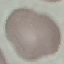
malaria status = uninfected
capture = smartphone through the microscope eyepiece
image type = cell patch, automatically extracted from a larger field of view and resized to 64 × 64 pixels
preparation = thin smear
stain = Giemsa